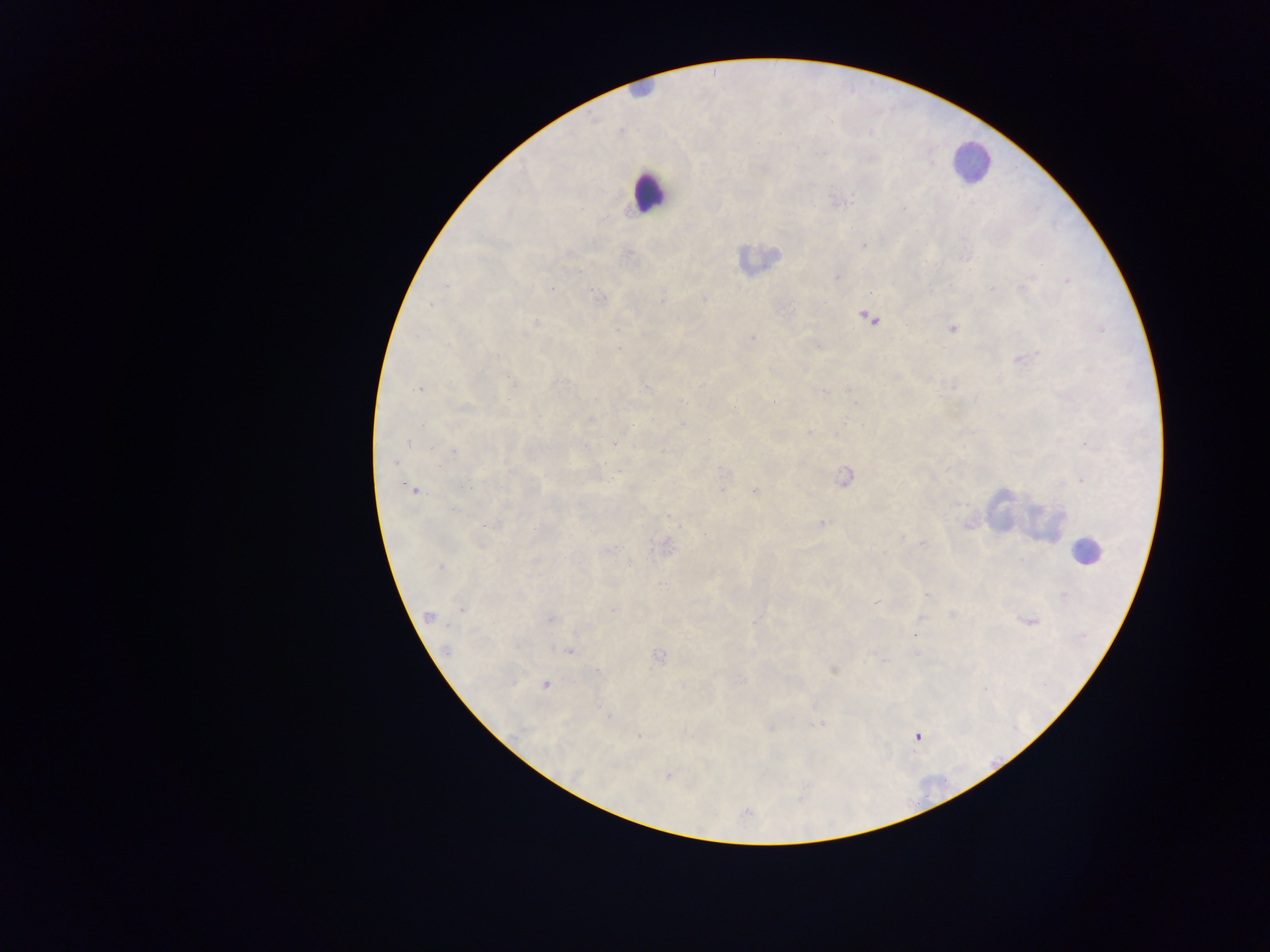

leukocyte locations = approximate centers as [x, y] in pixels: [641, 91], [970, 162], [647, 192], [758, 260], [1088, 552]
Plasmodium parasite locations = approximate centers as [x, y] in pixels: [620, 131], [839, 201], [863, 246], [628, 254], [836, 276], [1067, 280], [601, 297], [703, 297], [867, 318], [534, 322], [952, 328], [751, 337], [1022, 358], [648, 387], [773, 401], [685, 402], [733, 407], [588, 419], [682, 423], [616, 443], [394, 463], [620, 471], [844, 476], [1081, 479], [414, 489], [754, 492], [821, 523], [704, 536], [924, 543], [665, 547], [629, 564], [440, 568], [927, 595], [877, 601], [462, 608], [428, 617], [551, 619], [1028, 621], [916, 636], [569, 650], [916, 653], [658, 657], [885, 660], [833, 669], [545, 684], [816, 724], [771, 725], [638, 735], [917, 736], [667, 774], [745, 813]
image size = 1270×952 pixels
country = Ghana
preparation = thick blood smear
capture = mobile-phone photograph through a microscope
field of view = single